Identify the parasite.
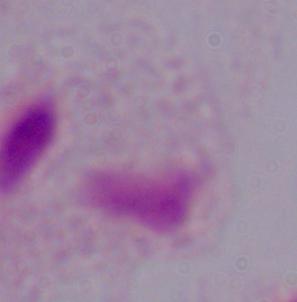
A trichomonad.

modality = micrograph
magnification = 1000x